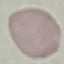

result = negative for malaria parasites
stain = Giemsa
preparation = thin blood smear
capture = smartphone through the microscope eyepiece
image type = cell patch, automatically extracted from a larger field of view and resized to 64 × 64 pixels